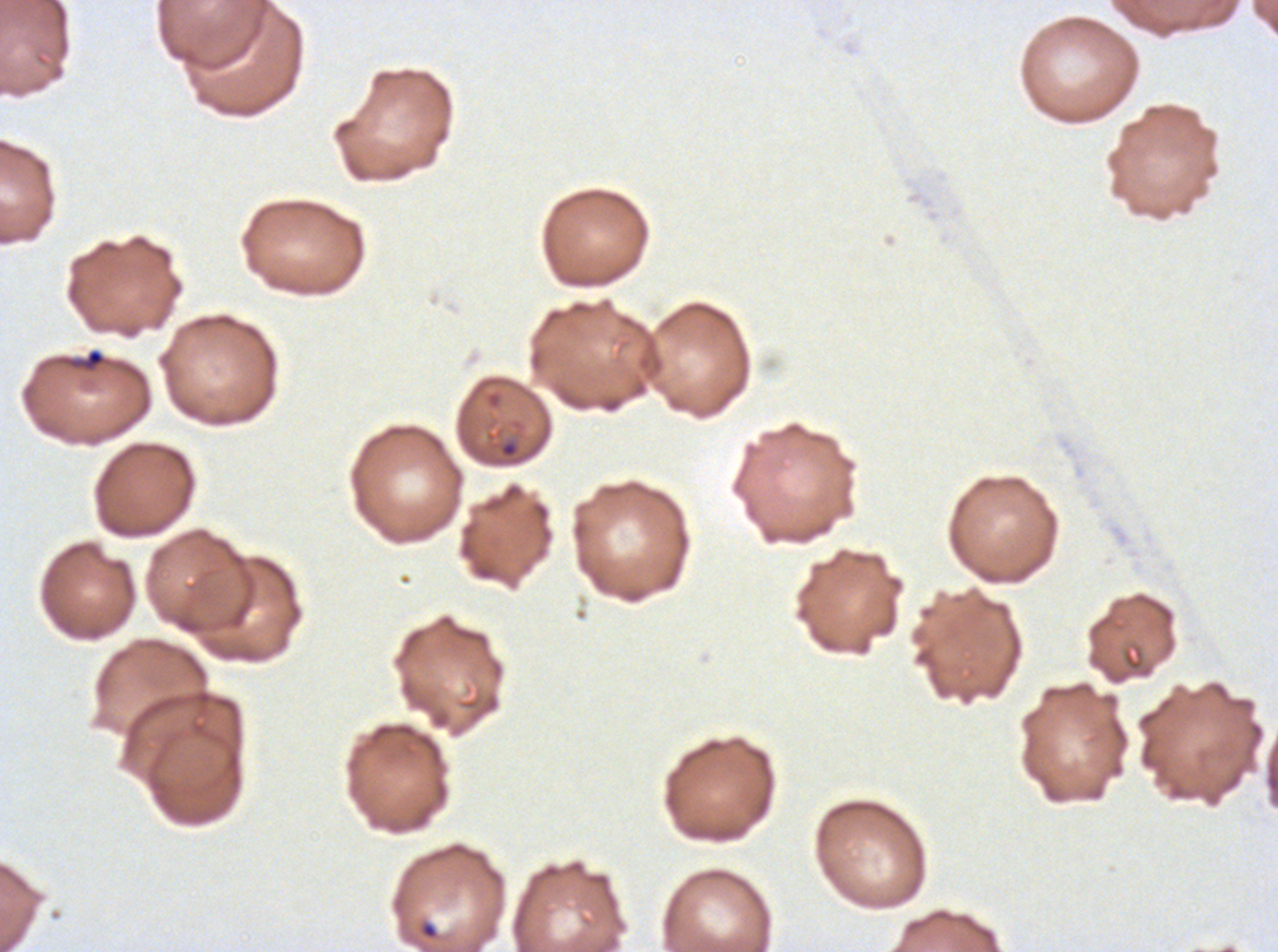
Approximate bounding boxes as (x1, y1, x2, y2) in pixels. Debris locations: (68, 348, 106, 372). Ring locations: (499, 441, 518, 458), (419, 920, 439, 941). Ex-vivo Plasmodium falciparum culture from a patient in The Gambia, grown for 24 to 48 hours. Giemsa-stained preparation. A sub-image separated from a larger composite. Image is 1278×952 pixels. Thin blood smear.